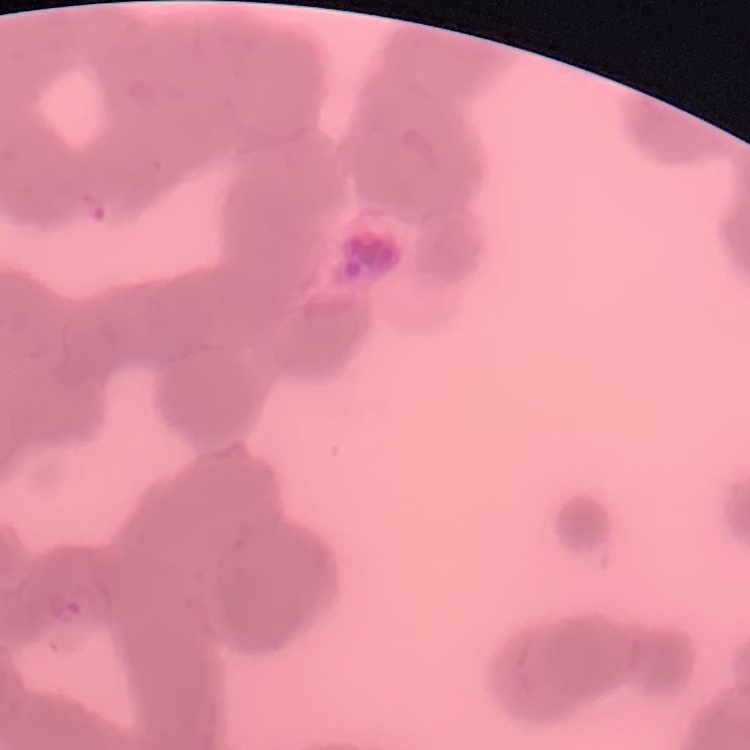

Summary:
  - Erythrocyte morphology: rouleaux formation
  - Image type: one tile cut from a larger photomicrograph
  - Preparation: thin blood film
  - Stain: Field's or Giemsa